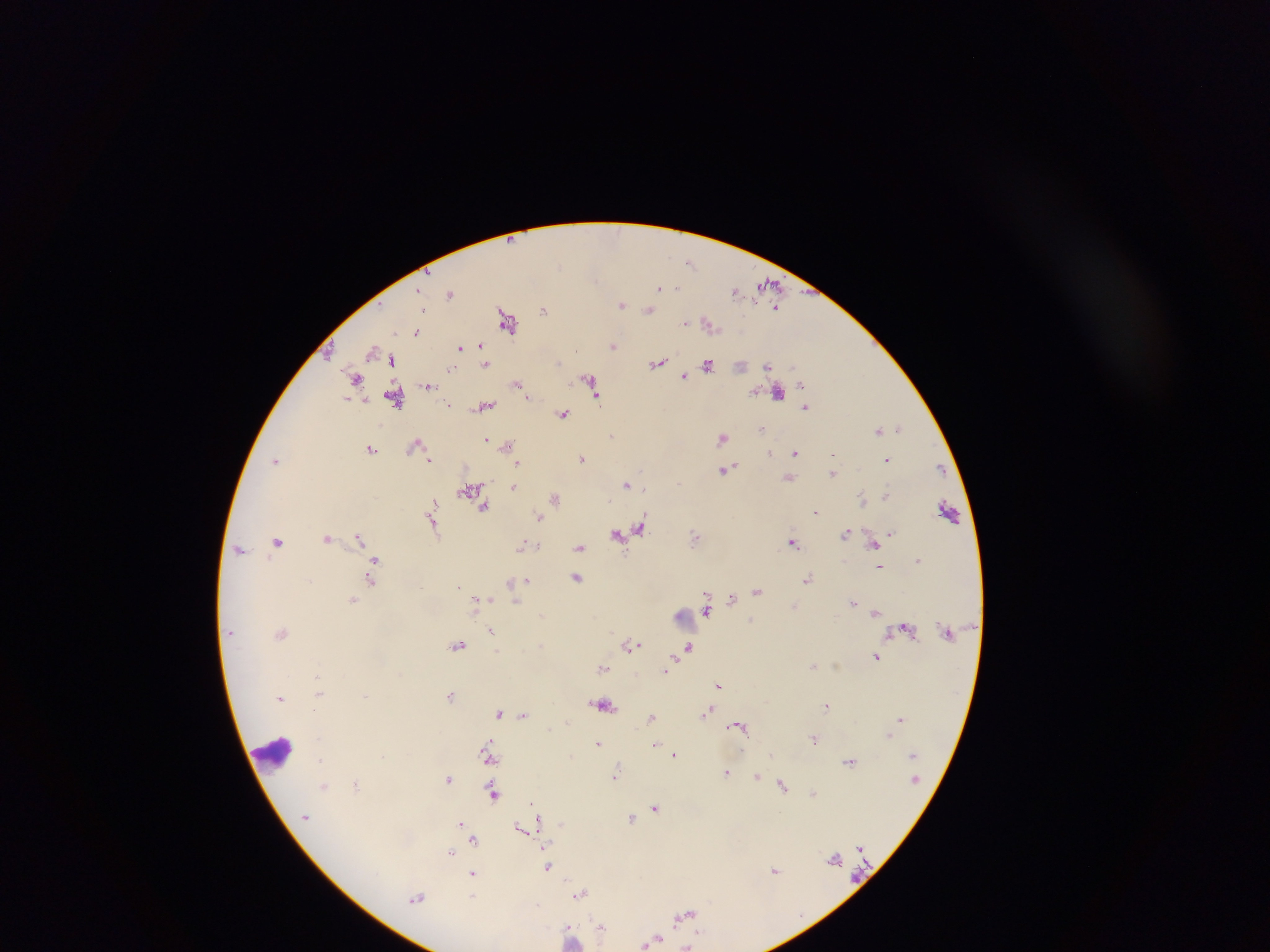 Approximate centers as x y in pixels. Malaria parasite locations: 690 262; 768 283; 659 287; 677 288; 735 290; 450 294; 622 305; 777 307; 544 309; 649 310; 422 311; 506 319; 685 323; 710 325; 417 332; 613 346; 481 347; 459 348; 374 350; 392 360; 657 363; 486 364; 707 365; 767 366; 452 368; 683 377; 589 378; 356 379; 429 384; 517 384; 801 385; 778 393; 596 397; 395 398; 449 404; 484 407; 805 407; 563 413; 900 427; 761 429; 879 429; 612 436; 722 438; 486 439; 506 445; 414 446; 371 449; 795 452; 770 454; 833 454; 582 458; 430 459; 886 460; 277 461; 517 463; 939 468; 642 470; 724 470; 833 473; 789 479; 626 485; 514 487; 470 488; 644 489; 886 495; 555 497; 863 500; 484 506; 433 507; 948 510; 816 511; 431 515; 539 516; 433 524; 641 528; 846 533; 890 533; 617 534; 695 536; 359 537; 327 538; 277 541; 793 543; 874 543; 522 545; 538 546; 580 547; 239 549; 919 559; 375 561; 879 565; 577 577; 808 579; 371 580; 526 580; 512 583; 459 587; 758 590; 732 599; 352 600; 482 600; 515 601; 854 602; 706 610; 876 613; 541 614; 752 621; 491 630; 282 632; 540 645; 631 645; 458 646; 688 647; 876 657; 813 666; 602 667; 666 669; 719 684; 318 693; 366 695; 451 696; 282 698; 603 704; 826 705; 707 712; 500 713; 523 714; 653 717; 900 718; 738 725; 889 736; 814 739; 598 743; 655 743; 772 754; 489 755; 674 755; 320 759; 850 762; 727 772; 615 775; 756 776; 448 778; 356 784; 324 786; 783 786; 493 792; 813 793; 532 804; 655 807; 305 817; 538 818; 631 818; 462 824; 521 827; 474 840; 451 852; 548 866; 775 870; 473 875; 580 893; 473 897; 417 898; 684 915; 601 927; 571 934; 652 940. Leukocyte locations: 685 619; 273 752. Image is 1270×952 pixels. Thick blood smear. Collected in Ghana. Single field of view. Mobile-phone photograph taken through the microscope.